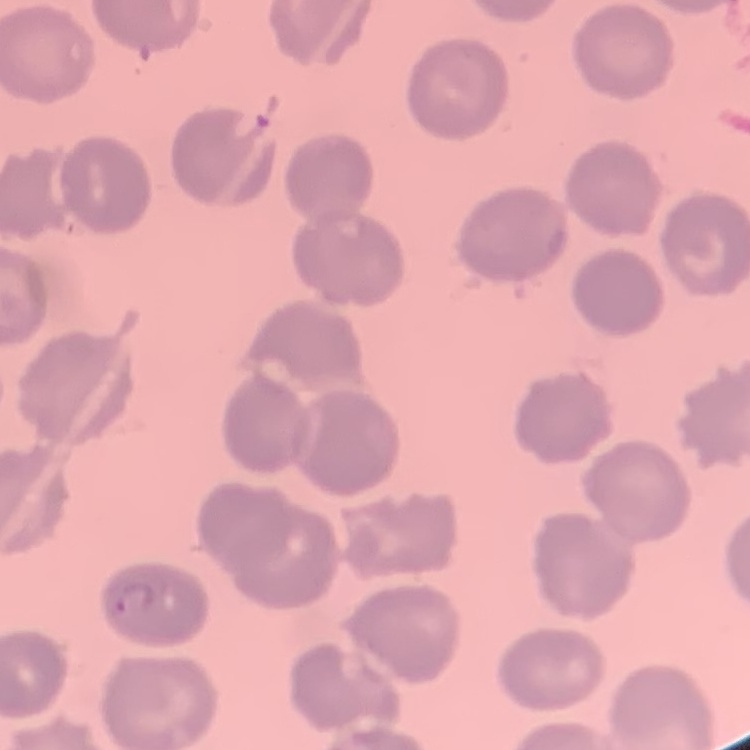
red blood cell morphology = no rouleaux formation
stain = Field's or Giemsa
image type = square crop of a larger photomicrograph
preparation = thin blood film